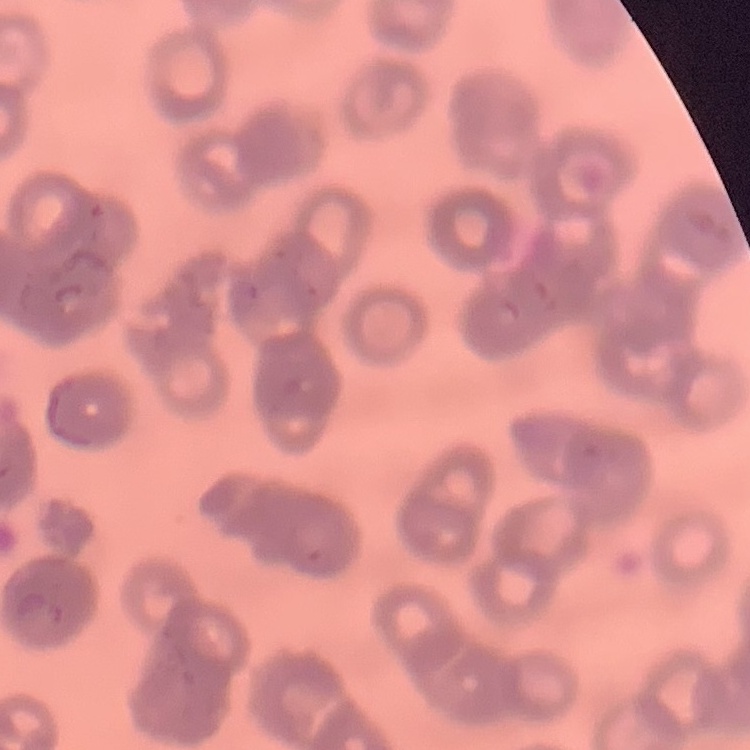 The red blood cells show rouleaux formation. Field's or Giemsa stain. Thin peripheral smear. One tile cut from a larger photomicrograph.